Give a bounding box for every artifact (stain precipitate or debris).
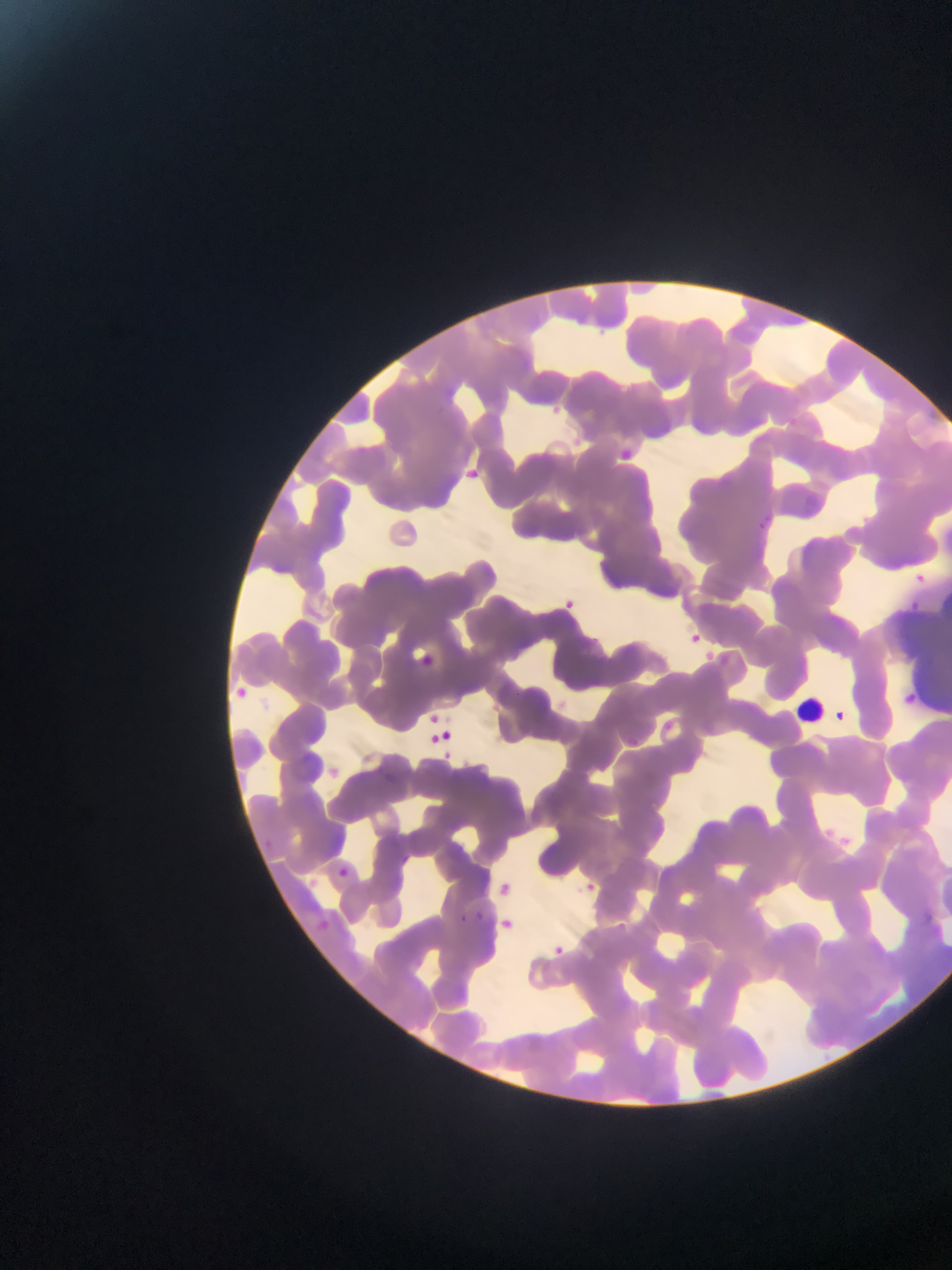

Approximate bounding boxes as [left, top, right, bottom] in pixels.
Artifacts (stain precipitate or debris): [892, 611, 952, 700].

country = Ghana
field of view = single
image size = 952×1270 pixels
capture = mobile-phone photograph through a microscope
preparation = thin blood smear
malaria parasite locations = approximate bounding boxes as [left, top, right, bottom] in pixels: [549, 399, 569, 420], [467, 467, 483, 489], [914, 566, 932, 588], [562, 592, 582, 619], [907, 598, 921, 615], [682, 630, 704, 650], [236, 678, 256, 696], [900, 693, 914, 711], [419, 708, 440, 720], [834, 710, 848, 722], [441, 723, 458, 743], [426, 734, 439, 748], [440, 750, 456, 760], [841, 834, 853, 851], [338, 868, 349, 877], [586, 882, 601, 888], [917, 911, 937, 925], [476, 912, 485, 920], [457, 913, 468, 924], [501, 919, 513, 929], [553, 940, 567, 958]